Give the position of every leukocyte visible.
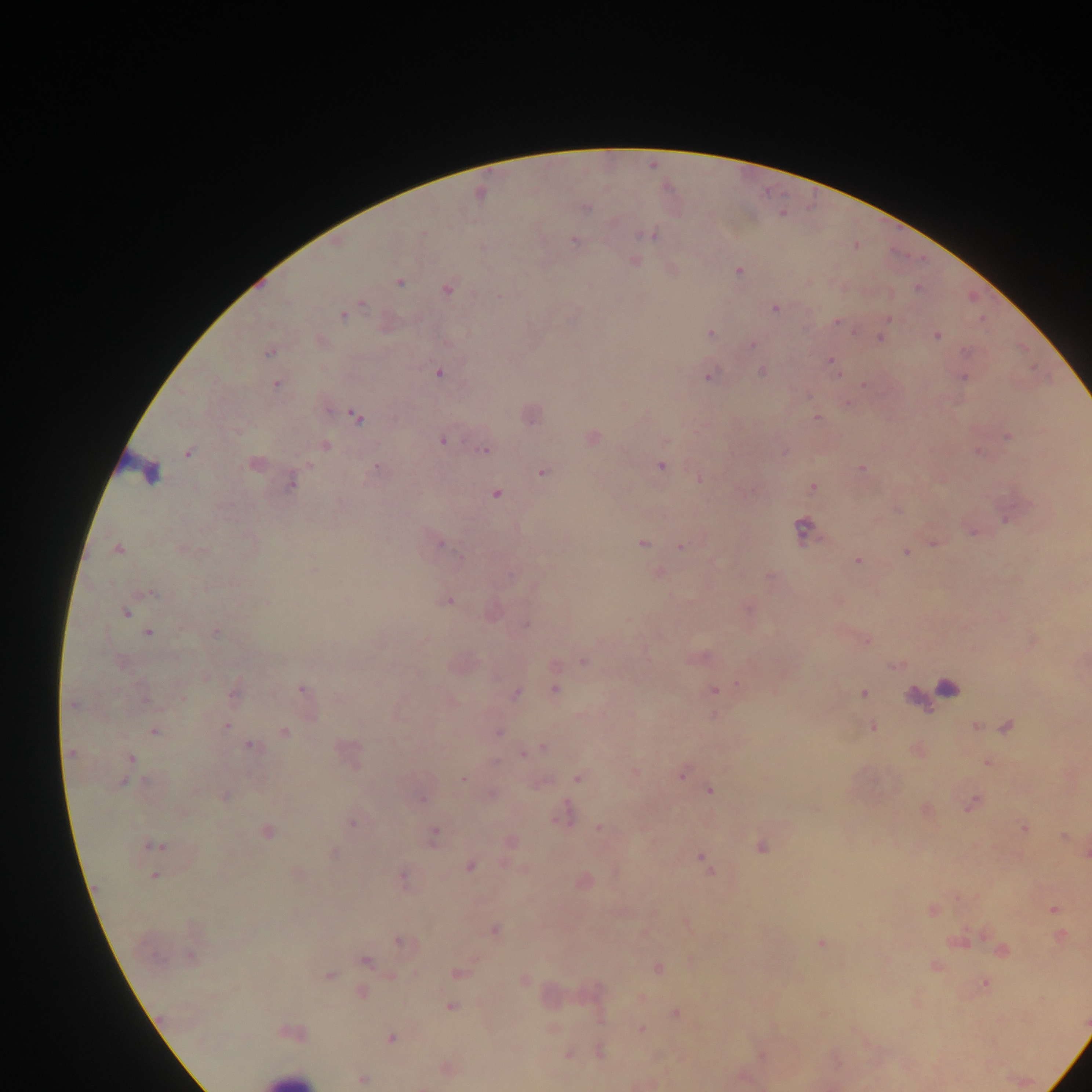
Approximate centers as {x, y} in pixels.
Leukocytes: {151, 475}, {286, 1079}.

image size = 1092×1092 pixels
malaria parasite locations = approximate centers as {x, y} in pixels: {587, 208}, {647, 235}, {573, 240}, {738, 271}, {399, 282}, {917, 287}, {448, 289}, {364, 304}, {775, 309}, {343, 316}, {888, 320}, {837, 322}, {711, 334}, {937, 335}, {881, 337}, {753, 345}, {965, 351}, {268, 353}, {830, 361}, {438, 372}, {762, 372}, {709, 377}, {964, 377}, {864, 383}, {276, 385}, {356, 416}, {816, 418}, {1008, 437}, {442, 440}, {326, 444}, {485, 451}, {979, 451}, {188, 453}, {376, 466}, {661, 466}, {863, 469}, {543, 472}, {699, 479}, {291, 483}, {813, 487}, {496, 494}, {803, 527}, {642, 544}, {441, 545}, {680, 547}, {180, 548}, {118, 549}, {905, 552}, {857, 560}, {313, 569}, {154, 593}, {449, 601}, {267, 602}, {748, 607}, {126, 613}, {527, 625}, {216, 632}, {149, 633}, {583, 662}, {738, 685}, {302, 689}, {713, 689}, {948, 689}, {556, 690}, {234, 692}, {863, 692}, {516, 694}, {182, 698}, {145, 700}, {72, 705}, {227, 726}, {1007, 726}, {872, 727}, {976, 727}, {154, 731}, {284, 732}, {498, 732}, {251, 745}, {543, 748}, {72, 753}, {523, 753}, {130, 758}, {988, 763}, {682, 775}, {463, 779}, {578, 779}, {147, 782}, {124, 783}, {710, 791}, {492, 794}, {224, 796}, {423, 799}, {974, 803}, {563, 817}, {352, 823}, {599, 828}, {1024, 828}, {266, 832}, {434, 833}, {511, 842}, {154, 846}, {761, 847}, {334, 853}, {701, 857}, {470, 866}, {154, 875}, {403, 879}, {1054, 909}, {933, 910}, {688, 925}, {495, 930}, {399, 942}, {821, 943}, {1002, 951}, {189, 955}, {365, 961}, {937, 966}, {658, 968}, {458, 973}, {329, 976}, {525, 981}, {985, 984}, {362, 993}, {451, 1007}, {676, 1013}, {641, 1029}, {292, 1032}, {391, 1038}, {599, 1050}, {568, 1055}, {446, 1068}, {363, 1079}
capture = mobile-phone photograph through a microscope
preparation = thick blood film
field of view = single
country = Ghana